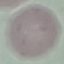

Malaria status: uninfected. Acquired by smartphone through the microscope eyepiece. Cell patch, automatically extracted from a larger field of view and resized to 64 × 64 pixels. Giemsa-stained preparation. Thin smear of blood.